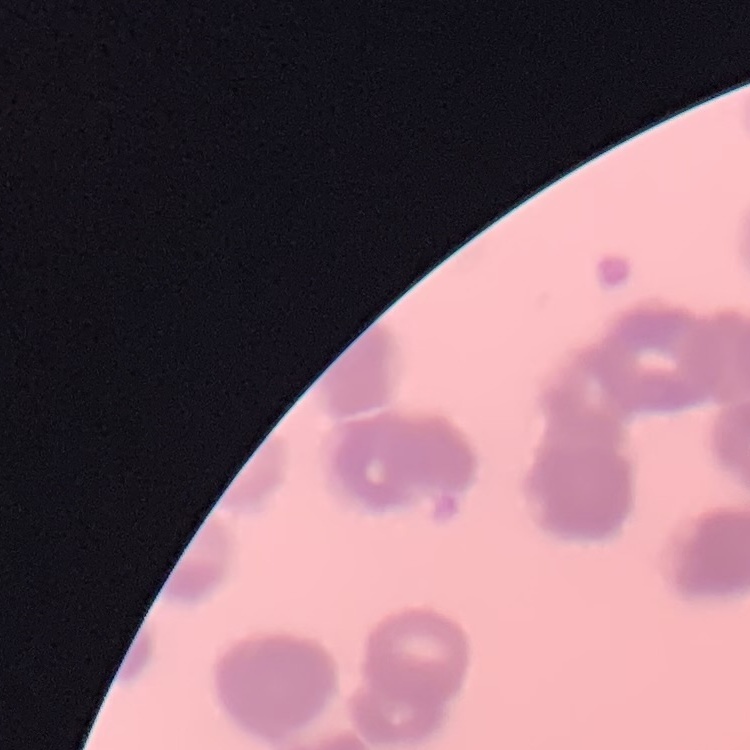
{
  "erythrocyte_morphology": "rouleaux formation",
  "image_type": "square crop of a larger photomicrograph",
  "stain": "Field's or Giemsa",
  "preparation": "thin blood film"
}